Outline platelets.
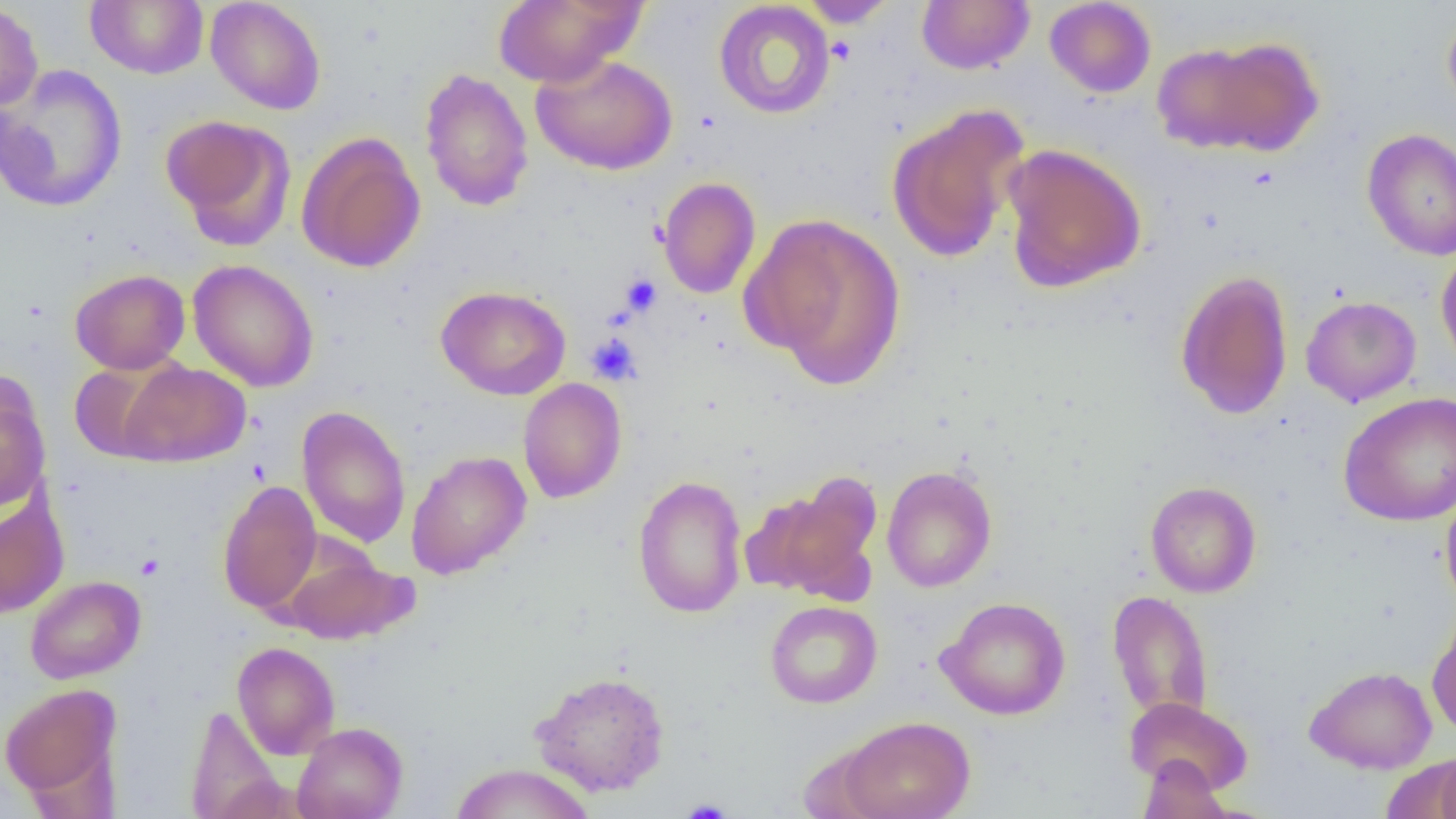
Approximate bounding boxes as named x1/y1/x2/y2 corners in pixels.
Platelets: (x1=620, y1=273, x2=662, y2=316), (x1=586, y1=333, x2=643, y2=385), (x1=136, y1=553, x2=164, y2=580), (x1=680, y1=799, x2=734, y2=819).

Uninfected red blood cell locations: (x1=85, y1=0, x2=209, y2=79), (x1=206, y1=0, x2=326, y2=115), (x1=493, y1=0, x2=644, y2=87), (x1=797, y1=0, x2=899, y2=27), (x1=917, y1=1, x2=1034, y2=74), (x1=1044, y1=1, x2=1157, y2=98), (x1=0, y1=2, x2=43, y2=112), (x1=713, y1=2, x2=835, y2=119), (x1=1442, y1=7, x2=1456, y2=120), (x1=1155, y1=35, x2=1323, y2=158), (x1=531, y1=55, x2=678, y2=175), (x1=1, y1=65, x2=128, y2=213), (x1=419, y1=67, x2=534, y2=212), (x1=885, y1=102, x2=1031, y2=264), (x1=160, y1=115, x2=295, y2=250), (x1=1362, y1=128, x2=1456, y2=261), (x1=296, y1=132, x2=426, y2=273), (x1=1001, y1=144, x2=1146, y2=293), (x1=657, y1=177, x2=761, y2=299), (x1=745, y1=214, x2=906, y2=386), (x1=1436, y1=245, x2=1456, y2=376), (x1=188, y1=259, x2=319, y2=392), (x1=70, y1=269, x2=190, y2=374), (x1=1174, y1=269, x2=1294, y2=420), (x1=435, y1=285, x2=571, y2=400), (x1=1300, y1=295, x2=1422, y2=407), (x1=69, y1=360, x2=180, y2=463), (x1=117, y1=360, x2=251, y2=467), (x1=518, y1=378, x2=627, y2=503), (x1=0, y1=381, x2=51, y2=510), (x1=1338, y1=391, x2=1456, y2=526), (x1=297, y1=406, x2=411, y2=547), (x1=406, y1=450, x2=531, y2=578), (x1=881, y1=465, x2=997, y2=592), (x1=747, y1=473, x2=885, y2=604), (x1=632, y1=475, x2=748, y2=618), (x1=217, y1=480, x2=321, y2=614), (x1=1145, y1=481, x2=1261, y2=598), (x1=1440, y1=487, x2=1456, y2=613), (x1=0, y1=496, x2=69, y2=619), (x1=281, y1=544, x2=415, y2=645), (x1=25, y1=575, x2=145, y2=683), (x1=1107, y1=589, x2=1213, y2=725), (x1=936, y1=596, x2=1071, y2=720), (x1=765, y1=601, x2=882, y2=708), (x1=1426, y1=612, x2=1456, y2=738), (x1=232, y1=642, x2=340, y2=759), (x1=1304, y1=665, x2=1437, y2=773), (x1=531, y1=670, x2=670, y2=797), (x1=0, y1=682, x2=122, y2=803), (x1=1124, y1=697, x2=1253, y2=795), (x1=185, y1=705, x2=284, y2=818), (x1=838, y1=715, x2=976, y2=819), (x1=293, y1=722, x2=408, y2=819), (x1=1435, y1=749, x2=1456, y2=819), (x1=1387, y1=754, x2=1456, y2=816), (x1=1136, y1=757, x2=1232, y2=818), (x1=448, y1=763, x2=595, y2=819). Slide-level diagnosis: negative for blood parasites. Light microscopy. Thin blood film. 1000x magnification. Image is 1456×819 pixels. Single field of view.